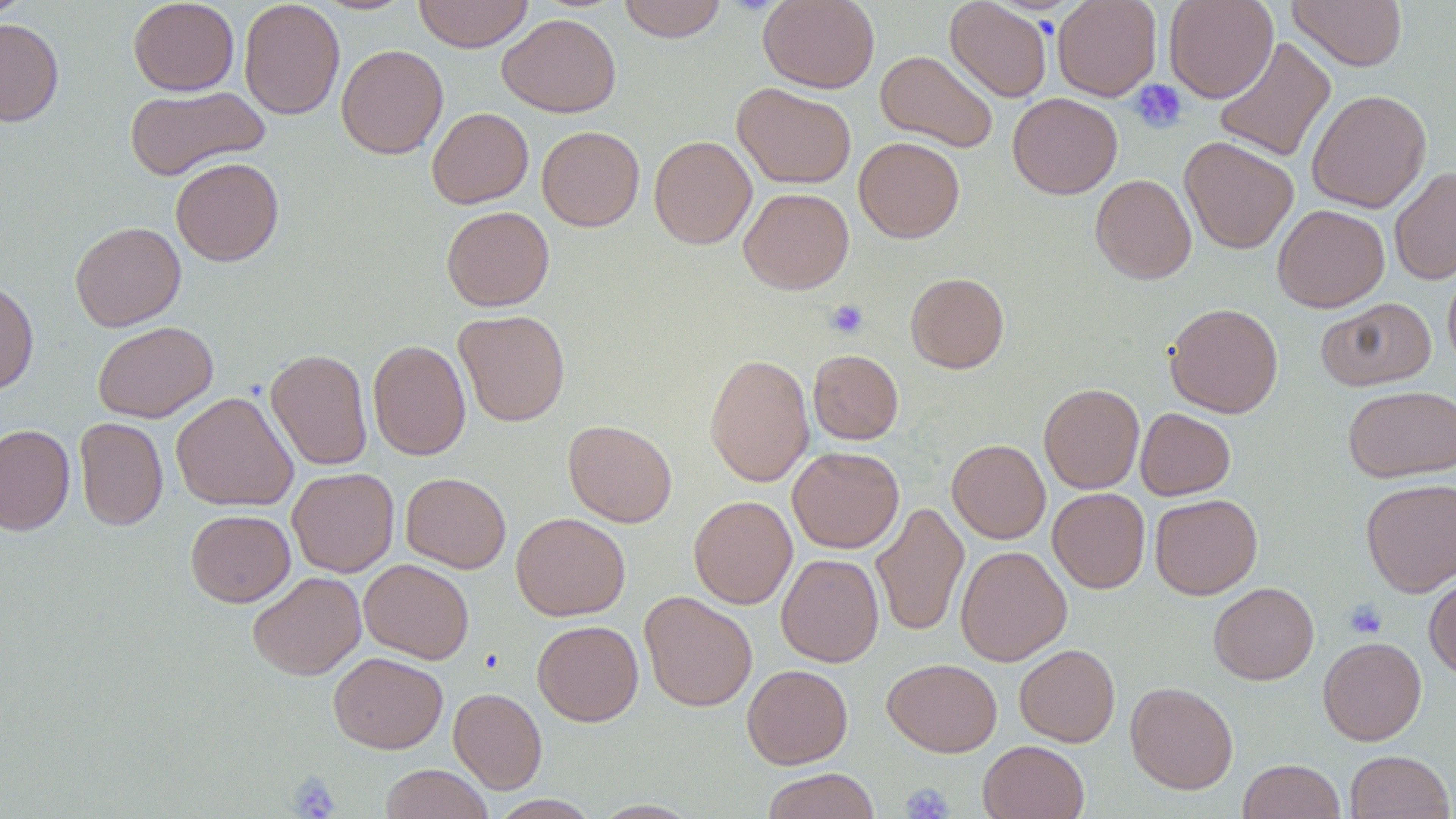

slide-level diagnosis = negative for blood parasites
uninfected red blood cell locations = approximate bounding boxes as [x1, y1, x2, y2] in pixels: [0, 0, 33, 23], [128, 0, 240, 96], [239, 0, 345, 120], [413, 0, 534, 52], [618, 0, 727, 42], [758, 0, 880, 92], [945, 0, 1052, 102], [1053, 0, 1161, 101], [1163, 0, 1278, 103], [1287, 0, 1407, 71], [497, 13, 621, 117], [0, 18, 64, 127], [1214, 37, 1336, 163], [336, 44, 448, 159], [875, 49, 999, 152], [732, 82, 856, 189], [124, 84, 270, 181], [1307, 89, 1432, 213], [1007, 93, 1122, 199], [426, 107, 533, 209], [537, 126, 644, 231], [649, 135, 756, 249], [1179, 136, 1298, 254], [854, 137, 965, 243], [170, 157, 283, 266], [1389, 165, 1456, 285], [1090, 174, 1196, 284], [739, 187, 854, 294], [1272, 204, 1389, 312], [441, 206, 554, 311], [69, 221, 186, 331], [1442, 263, 1456, 371], [906, 272, 1009, 373], [0, 279, 38, 394], [1317, 297, 1436, 391], [1165, 302, 1283, 418], [454, 309, 570, 427], [92, 321, 218, 423], [368, 339, 471, 460], [265, 348, 372, 470], [808, 350, 903, 444], [704, 353, 814, 487], [1039, 383, 1144, 493], [1343, 385, 1456, 482], [171, 391, 298, 512], [1135, 408, 1235, 500], [74, 417, 168, 531], [563, 419, 677, 527], [0, 424, 75, 536], [947, 439, 1050, 543], [788, 446, 904, 553], [287, 468, 399, 577], [400, 472, 511, 573], [1360, 478, 1456, 597], [1048, 487, 1150, 593], [1150, 493, 1262, 599], [689, 495, 797, 609], [871, 501, 969, 638], [185, 509, 295, 607], [511, 512, 630, 620], [955, 545, 1072, 666], [776, 553, 884, 667], [359, 559, 474, 664], [247, 571, 366, 680], [1424, 573, 1456, 680], [1208, 582, 1319, 684], [639, 591, 757, 712], [532, 620, 643, 726], [1318, 637, 1427, 745], [1014, 643, 1120, 747], [328, 652, 448, 753], [882, 658, 1002, 756], [742, 664, 853, 768], [1125, 681, 1238, 794], [448, 687, 547, 794], [978, 740, 1089, 819], [1345, 750, 1455, 818], [1237, 759, 1346, 819], [380, 764, 493, 819], [761, 769, 880, 819]
field of view = one of a larger specimen
platelet locations = approximate bounding boxes as [x1, y1, x2, y2] in pixels: [1129, 79, 1187, 133], [825, 299, 869, 339], [1344, 598, 1387, 639], [288, 771, 341, 818], [901, 783, 954, 818]
stain = May-Grünwald-Giemsa
preparation = thin blood smear
image size = 1456×819 pixels
magnification = 1000x
modality = light microscopy